Describe the morphology of the erythrocytes.
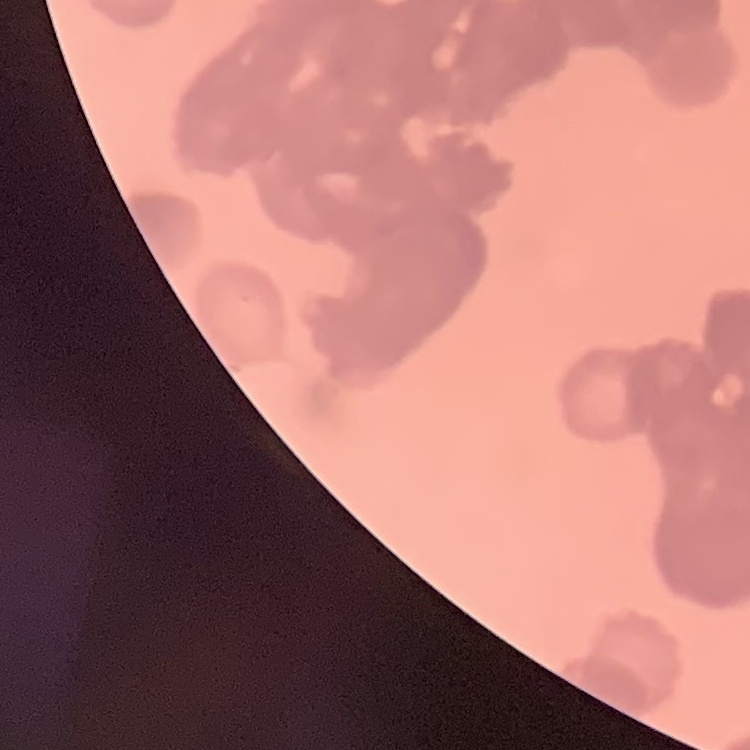
They show rouleaux formation.

preparation = thin peripheral smear
image type = one tile cut from a larger photomicrograph
stain = Field's or Giemsa